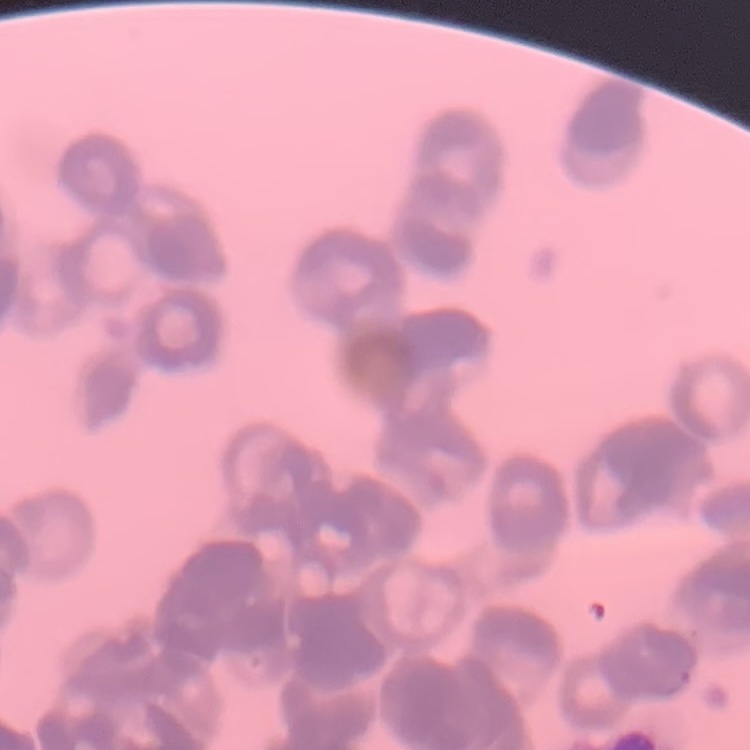

{
  "erythrocyte_morphology": "rouleaux formation",
  "image_type": "one tile cut from a larger photomicrograph",
  "stain": "Field's or Giemsa",
  "preparation": "thin peripheral smear"
}